Report the malaria status of this cell.
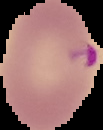

Parasitized.

From a thin blood smear. Image is 103×130 pixels. Segmented cell region on a black background.